Locate every blood parasite and identify its species.
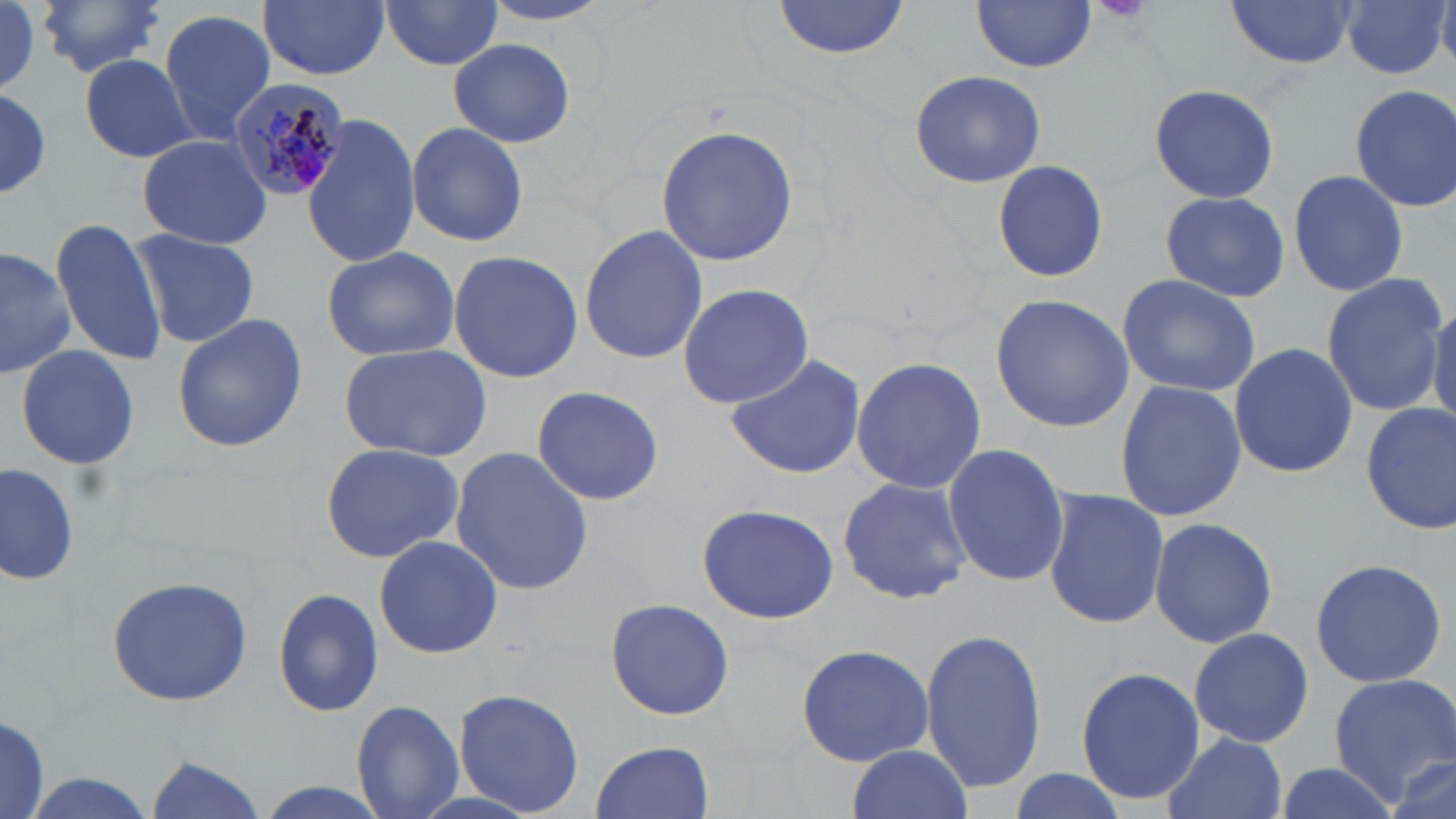
Approximate bounding boxes as [x1, y1, x2, y2] in pixels.
Plasmodium malariae-infected red blood cells: [224, 76, 351, 203].
No Plasmodium falciparum, Plasmodium ovale, Plasmodium vivax, Babesia divergens, or Trypanosoma brucei observed.

slide-level diagnosis = Plasmodium malariae
uninfected red blood cell locations = approximate bounding boxes as [x1, y1, x2, y2] in pixels: [36, 0, 168, 79], [259, 0, 389, 79], [1341, 0, 1452, 81], [772, 1, 918, 59], [971, 1, 1098, 72], [1223, 1, 1360, 70], [379, 2, 505, 70], [1, 4, 43, 96], [158, 8, 277, 143], [448, 37, 576, 148], [81, 54, 195, 163], [909, 68, 1046, 189], [1147, 83, 1281, 203], [1348, 84, 1456, 212], [0, 88, 52, 200], [299, 114, 420, 271], [405, 122, 527, 247], [655, 124, 802, 268], [136, 135, 271, 248], [990, 159, 1109, 284], [1286, 168, 1410, 298], [1157, 190, 1294, 302], [50, 216, 165, 366], [579, 224, 708, 364], [126, 228, 261, 349], [0, 243, 74, 379], [321, 245, 461, 362], [447, 250, 584, 383], [1319, 272, 1451, 417], [1117, 275, 1261, 396], [678, 282, 815, 410], [990, 292, 1137, 434], [1429, 298, 1456, 431], [171, 314, 307, 453], [1228, 341, 1356, 479], [339, 344, 490, 460], [13, 345, 141, 471], [723, 352, 867, 479], [851, 356, 987, 495], [1113, 378, 1246, 524], [532, 385, 664, 505], [1359, 401, 1456, 536], [318, 442, 466, 565], [942, 444, 1071, 587], [449, 445, 592, 596], [2, 462, 79, 588], [836, 477, 974, 605], [1041, 488, 1170, 629], [695, 503, 840, 624], [1147, 516, 1279, 649], [372, 535, 503, 659], [1308, 558, 1446, 688], [106, 573, 255, 707], [274, 586, 383, 719], [604, 596, 736, 720], [919, 626, 1047, 794], [1189, 627, 1314, 749], [795, 641, 935, 767], [1076, 666, 1205, 804], [1328, 672, 1455, 796], [451, 687, 586, 815], [348, 699, 464, 819], [0, 713, 50, 818], [1162, 731, 1285, 819], [591, 739, 715, 819], [843, 747, 973, 819], [145, 756, 267, 818], [1385, 756, 1454, 818], [1267, 761, 1403, 819], [1005, 769, 1131, 819], [13, 775, 163, 819], [250, 782, 393, 819]
modality = light microscopy
stain = May-Grünwald-Giemsa
preparation = thin blood smear
image size = 1456×819 pixels
field of view = single
magnification = 1000x